Comment on the morphology of the erythrocytes.
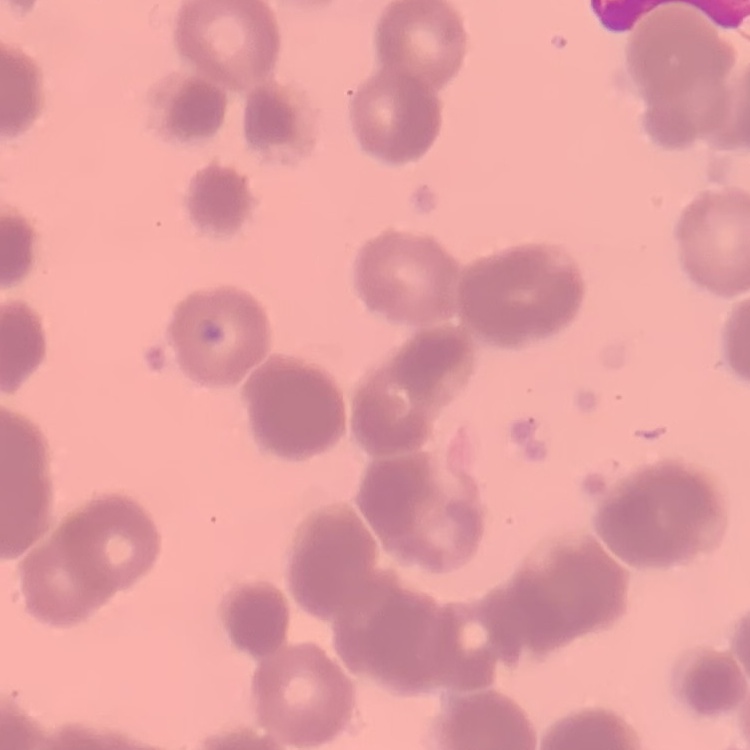

They show rouleaux formation.

Field's or Giemsa stain. Thin blood film. Square crop of a larger photomicrograph.